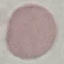

Summary:
  - Malaria status: uninfected
  - Stain: Giemsa
  - Preparation: thin blood film
  - Image type: automatically extracted cell patch, resized to 64 × 64 pixels
  - Capture: smartphone through the microscope eyepiece